Assess for parasitized red blood cells.
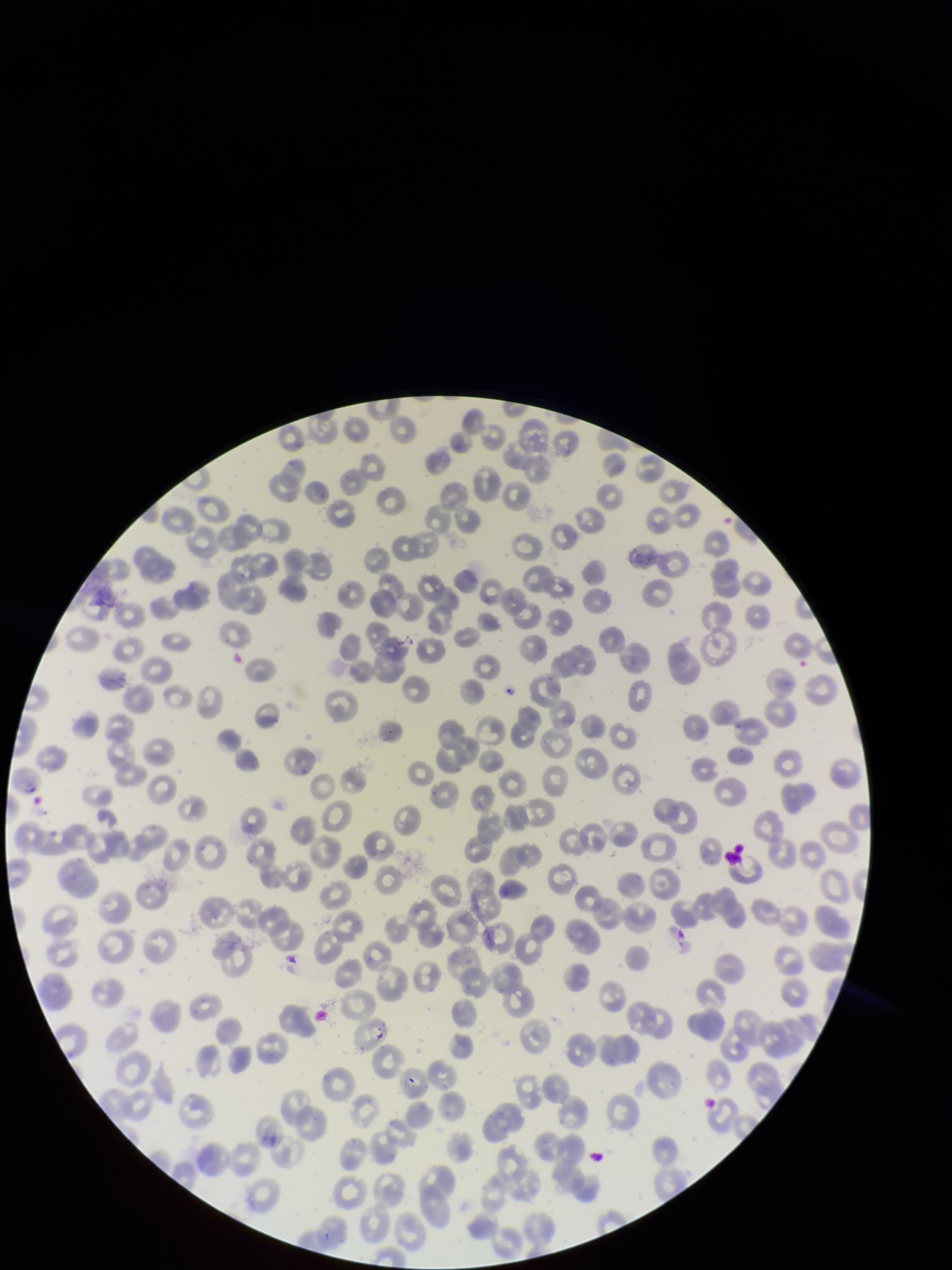

Seen.

Summary:
  - Stain: Giemsa
  - Red blood cell count: 237
  - Image size: 952×1270 pixels
  - Parasitized red blood cell count: 1
  - Species reported for this patient: Plasmodium falciparum
  - Capture: smartphone photograph through the microscope eyepiece
  - Field of view: one from this slide
  - Preparation: thin smear
  - Patient malaria status: infected